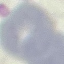

Summary:
  - Result: negative for malaria parasites
  - Preparation: thin blood smear
  - Capture: smartphone camera at the microscope eyepiece
  - Image type: cell patch, automatically extracted from a larger field of view and resized to 64 × 64 pixels
  - Stain: Giemsa